Name the parasite shown.
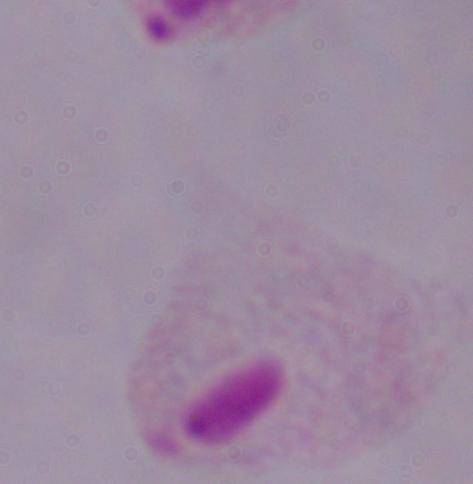
This is a trichomonad.

Micrograph. Captured at 1000x magnification.